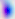

Summary:
  - Modality: micrograph
  - Magnification: 400x
  - Identification: Toxoplasma gondii